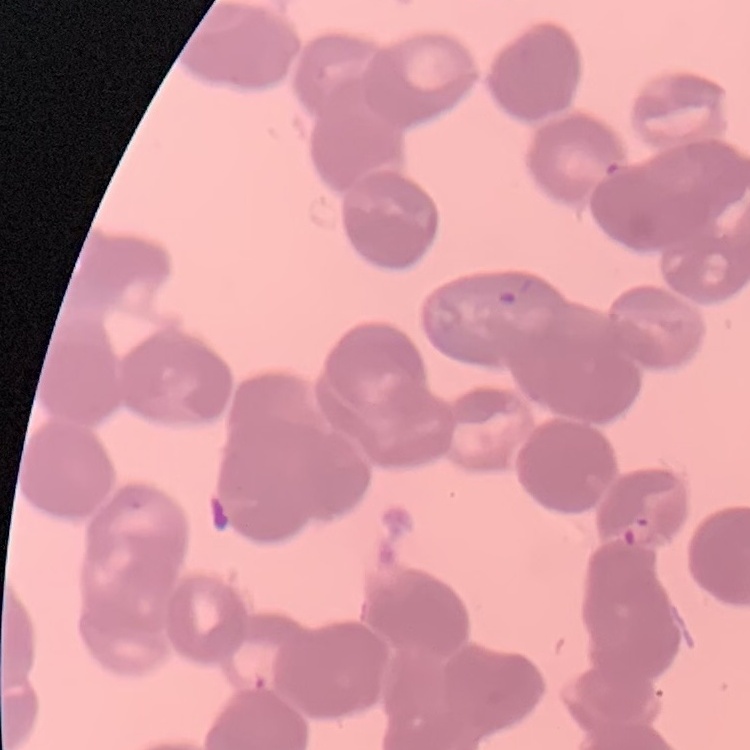

{
  "red_blood_cell_morphology": "rouleaux formation",
  "image_type": "square crop of a larger photomicrograph",
  "preparation": "thin blood film",
  "stain": "Field's or Giemsa"
}